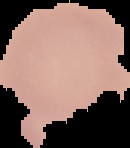

Summary:
  - Preparation: thin blood film
  - Image type: segmented cell region on a black background
  - Malaria status: uninfected
  - Image size: 130×148 pixels